Locate every leukocyte (white blood cell).
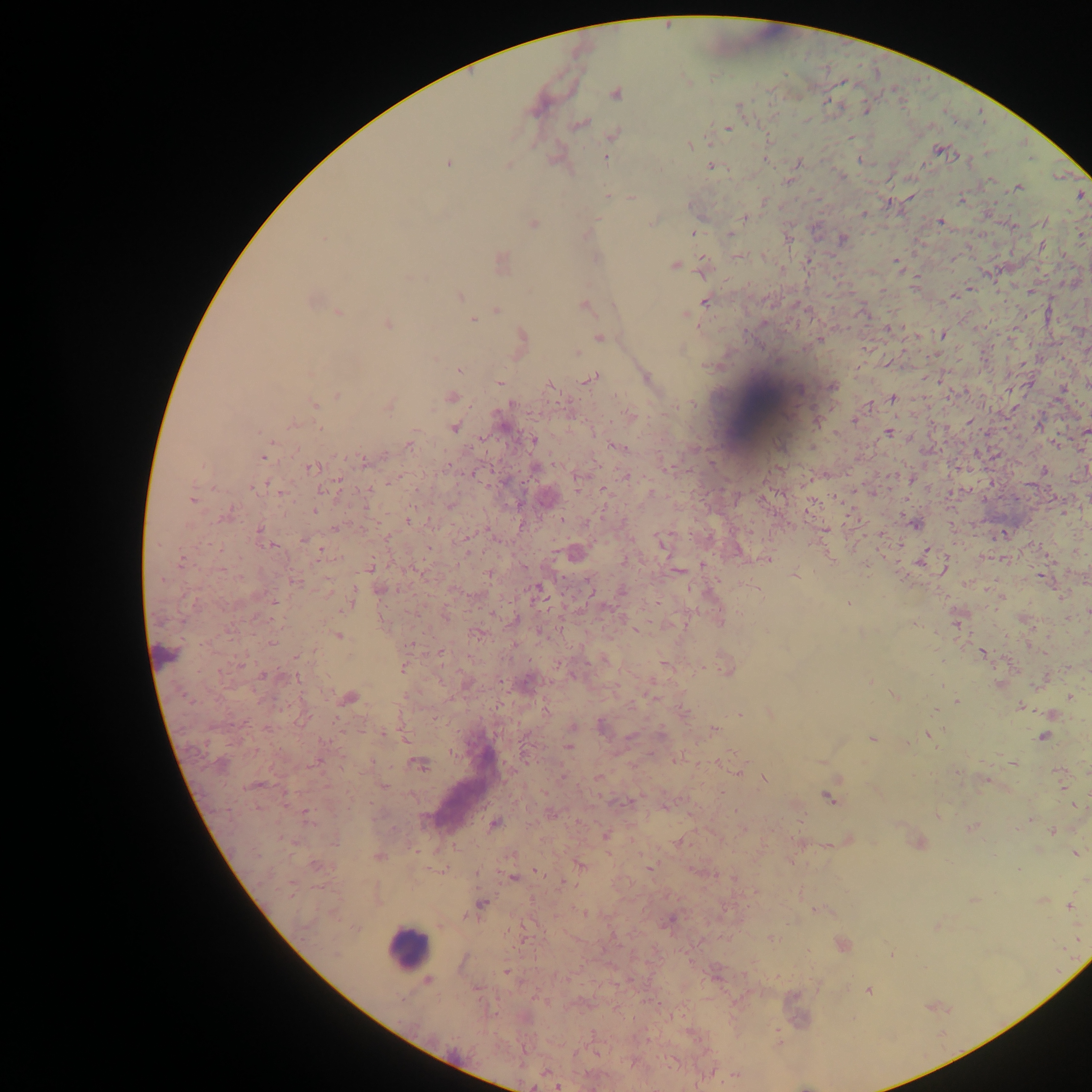
Approximate centers as (x, y) in pixels.
Leukocytes: (762, 405), (408, 948).

preparation = thick blood smear
image size = 1092×1092 pixels
capture = mobile-phone photograph through a microscope
field of view = single
country = Ghana
malaria parasite locations = approximate centers as (x, y) in pixels: (616, 93), (866, 109), (581, 124), (727, 129), (615, 134), (690, 145), (938, 149), (606, 158), (765, 159), (860, 160), (798, 163), (448, 164), (507, 165), (710, 166), (991, 179), (788, 181), (1018, 188), (1081, 195), (607, 196), (632, 198), (962, 199), (690, 206), (864, 214), (744, 217), (940, 222), (1043, 222), (652, 223), (533, 224), (693, 232), (729, 234), (587, 235), (1081, 237), (323, 238), (842, 240), (1041, 246), (597, 258), (702, 260), (896, 261), (502, 262), (674, 265), (410, 278), (460, 296), (311, 301), (705, 301), (583, 306), (614, 306), (496, 309), (338, 313), (686, 315), (472, 320), (388, 323), (889, 328), (942, 335), (522, 336), (599, 337), (820, 340), (576, 353), (459, 370), (646, 377), (591, 378), (500, 382), (550, 384), (832, 387), (798, 389), (337, 396), (451, 397), (892, 399), (314, 405), (511, 405), (867, 406), (389, 407), (629, 416), (855, 420), (294, 423), (454, 428), (1086, 431), (889, 432), (532, 441), (409, 443), (1056, 444), (615, 446), (262, 458), (363, 461), (313, 467), (1043, 470), (625, 475), (911, 478), (254, 488), (325, 489), (280, 492), (192, 499), (315, 511), (227, 514), (409, 520), (915, 525), (335, 529), (259, 530), (1003, 533), (303, 539), (662, 543), (320, 553), (923, 557), (181, 560), (766, 560), (370, 566), (489, 574), (795, 575), (163, 580), (296, 582), (538, 587), (380, 589), (622, 591), (351, 600), (848, 603), (516, 620), (957, 620), (721, 622), (635, 630), (474, 633), (338, 635), (271, 642), (983, 653), (664, 664), (403, 668), (727, 668), (262, 675), (870, 681), (527, 682), (895, 695), (1069, 696), (350, 697), (188, 699), (956, 701), (1020, 707), (685, 713), (769, 713), (739, 714), (602, 727), (713, 730), (383, 733), (928, 734), (660, 735), (630, 737), (1043, 737), (871, 739), (569, 747), (679, 758), (719, 762), (419, 764), (1013, 764), (739, 768), (597, 778), (764, 779), (985, 781), (257, 785), (383, 786), (827, 797), (306, 813), (551, 813), (1030, 820), (493, 825), (972, 827), (1052, 831), (605, 837), (848, 840), (919, 843), (1076, 853), (378, 857), (316, 865), (581, 865), (649, 867), (537, 872), (513, 878), (973, 900), (1042, 901), (482, 903), (1070, 906), (585, 913), (670, 919), (771, 938), (843, 945), (891, 954), (507, 971), (428, 980), (869, 990), (546, 1072), (736, 1075), (558, 1087)